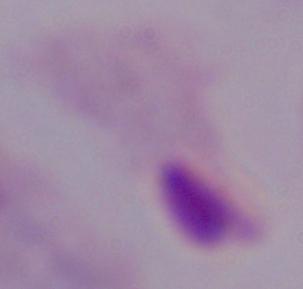

Micrograph. A trichomonad is seen. Captured at 1000x magnification.